Identify the cell.
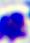

This is a leukocyte.

Captured at 400x magnification. Micrograph.